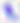

Summary:
  - Identification: Toxoplasma gondii
  - Magnification: 400x
  - Modality: micrograph